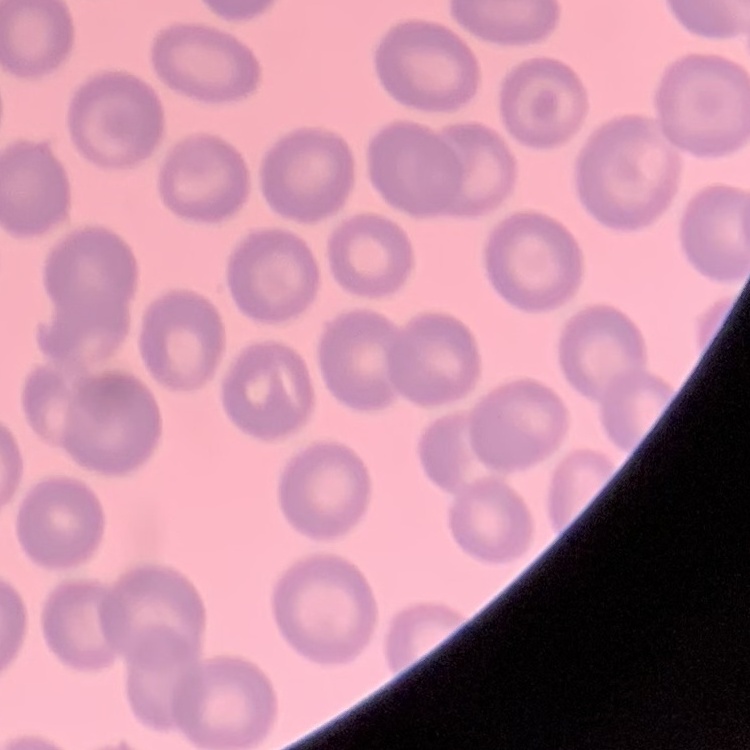
erythrocyte_morphology: no rouleaux formation
preparation: thin blood smear
stain: Field's or Giemsa
image_type: one tile cut from a larger photomicrograph